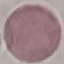
malaria status = uninfected
preparation = thin blood smear
capture = smartphone camera at the microscope eyepiece
image type = cell patch, automatically extracted from a larger field of view and resized to 64 × 64 pixels
stain = Giemsa